Identify the blood parasite species.
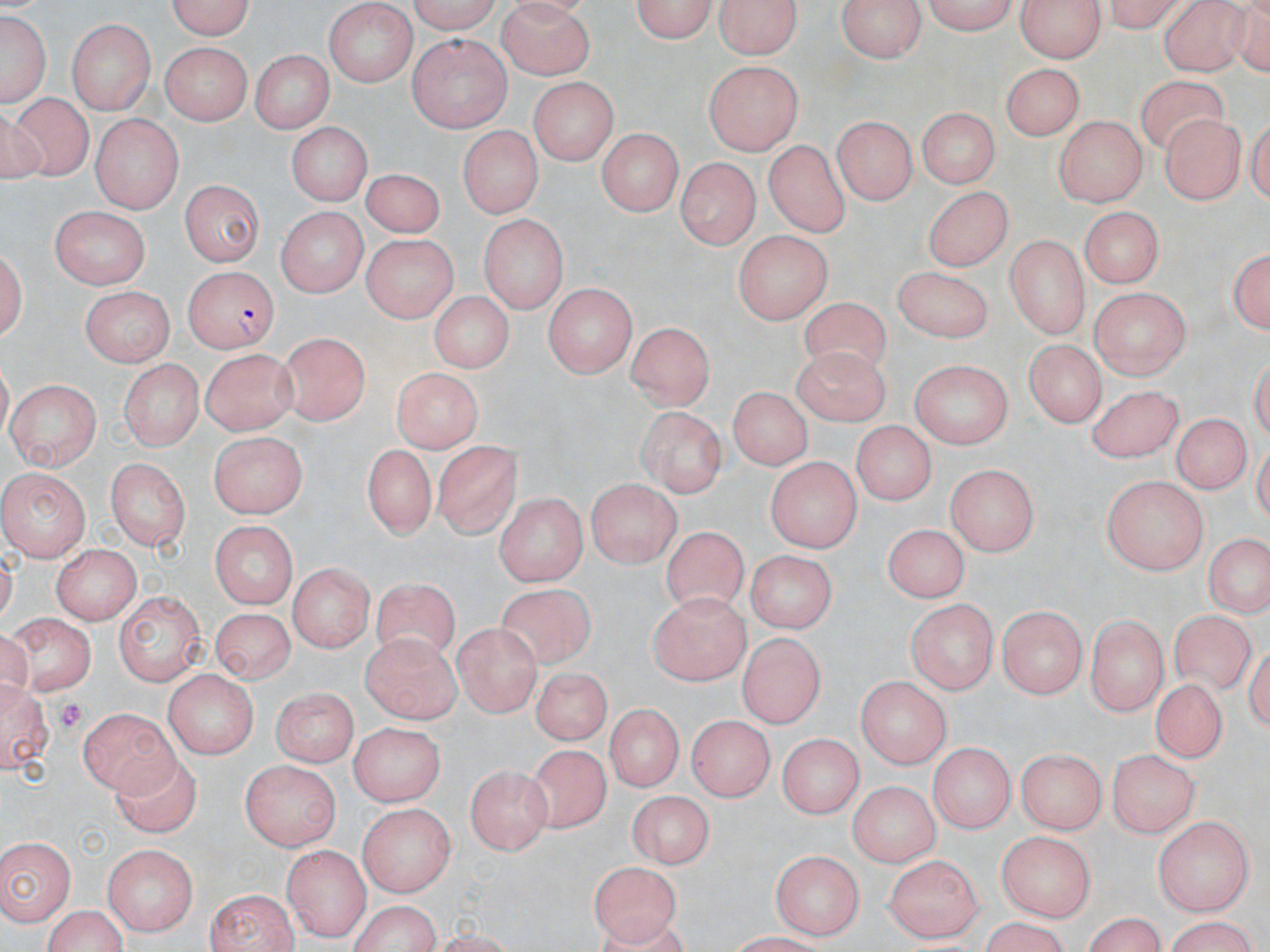
Plasmodium falciparum.

Approximate bounding boxes as (x1,y1)-(x2,y2) corner pairs in pixels. Platelet locations: (50,697)-(88,735). Uninfected red blood cell locations: (165,0)-(259,39), (402,0)-(502,32), (628,0)-(723,44), (713,0)-(805,59), (834,0)-(929,64), (921,0)-(1020,33), (1019,0)-(1103,65), (493,2)-(595,77), (1105,2)-(1186,33), (326,3)-(416,87), (1157,4)-(1259,76), (0,7)-(52,109), (68,18)-(154,112), (409,35)-(512,131), (161,42)-(252,125), (250,48)-(333,137), (706,61)-(801,156), (1000,64)-(1082,142), (1128,74)-(1227,154), (528,76)-(620,166), (4,89)-(98,184), (915,106)-(998,190), (834,113)-(917,204), (90,114)-(180,210), (1051,116)-(1148,204), (1158,118)-(1245,204), (286,124)-(368,206), (455,125)-(545,218), (595,130)-(686,215), (763,139)-(850,238), (677,158)-(760,247), (359,169)-(444,242), (178,180)-(267,264), (926,188)-(1010,270), (49,205)-(150,290), (1082,207)-(1164,284), (275,208)-(369,295), (480,216)-(566,313), (1004,231)-(1085,336), (364,232)-(462,321), (729,232)-(832,326), (2,239)-(28,350), (1225,241)-(1270,341), (892,264)-(996,345), (543,281)-(638,380), (1090,287)-(1190,379), (82,290)-(175,364), (429,290)-(516,377), (799,295)-(895,374), (624,322)-(717,410), (275,332)-(370,426), (1025,336)-(1105,426), (794,342)-(892,421), (200,349)-(298,436), (117,359)-(202,453), (908,359)-(1010,447), (389,367)-(486,451), (5,380)-(102,467), (1087,382)-(1182,462), (725,387)-(816,469), (637,403)-(728,500), (1171,412)-(1248,494), (849,422)-(937,506), (208,432)-(308,520), (430,439)-(520,541), (359,447)-(440,542), (768,454)-(861,550), (106,456)-(191,548), (946,463)-(1039,558), (4,468)-(91,563), (1100,475)-(1210,573), (587,477)-(678,566), (493,495)-(590,583), (211,518)-(301,606), (881,523)-(970,604), (658,527)-(746,614), (1198,536)-(1270,621), (51,545)-(140,625), (749,548)-(836,635), (291,564)-(373,654), (372,583)-(459,672), (496,585)-(601,672), (649,591)-(746,683), (113,593)-(208,682), (908,599)-(999,693), (995,605)-(1086,697), (212,607)-(290,684), (1170,609)-(1257,697), (1088,614)-(1169,711), (5,615)-(96,693), (454,622)-(541,714), (360,630)-(460,722), (739,635)-(826,728), (162,669)-(259,756), (526,670)-(617,746), (1154,675)-(1224,762), (0,678)-(54,776), (857,678)-(950,770), (274,685)-(359,766), (80,705)-(177,793), (606,706)-(682,792), (690,712)-(777,800), (351,720)-(446,807), (773,731)-(867,818), (929,741)-(1013,834), (522,744)-(614,833), (1019,746)-(1107,831), (1109,748)-(1199,837), (108,753)-(203,836), (241,762)-(340,851), (465,765)-(553,853), (849,780)-(939,867), (626,791)-(714,868), (357,801)-(456,898), (1154,818)-(1253,914), (998,832)-(1097,920), (0,836)-(75,925), (102,840)-(201,932), (281,844)-(366,936), (770,847)-(863,937), (887,855)-(980,941), (586,860)-(683,946), (203,888)-(299,951), (344,899)-(444,952), (41,905)-(131,952), (1077,915)-(1169,950), (1158,919)-(1264,951), (971,921)-(1078,950). Plasmodium falciparum-infected red blood cell locations: (182,265)-(277,353). Thin blood film. May-Grünwald-Giemsa-stained preparation. 1000x magnification. Single field of view. Optical microscopy. Image is 1270×952 pixels.